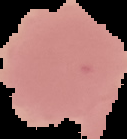
Result: malaria parasites identified. Image is 127×139 pixels. The area outside the segmented cell region is set to black. From a thin blood film.